Report the malaria status of this cell.
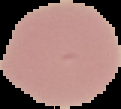

It is uninfected.

Summary:
  - Image type: segmented cell region on a black background
  - Preparation: thin blood smear
  - Image size: 121×109 pixels